Assess the morphology of the erythrocytes.
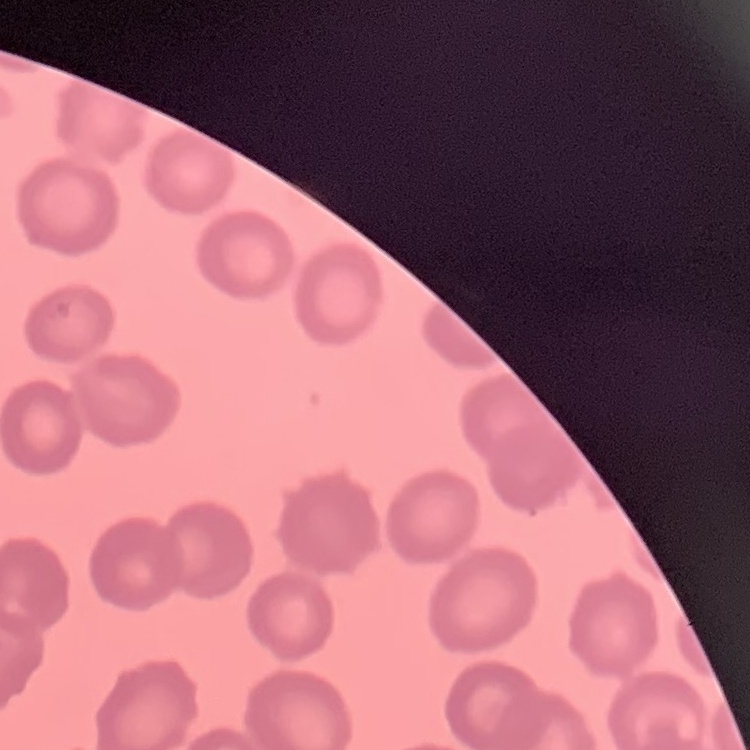

No rouleaux formation.

Summary:
  - Image type: square crop of a larger photomicrograph
  - Preparation: thin blood smear
  - Stain: Field's or Giemsa